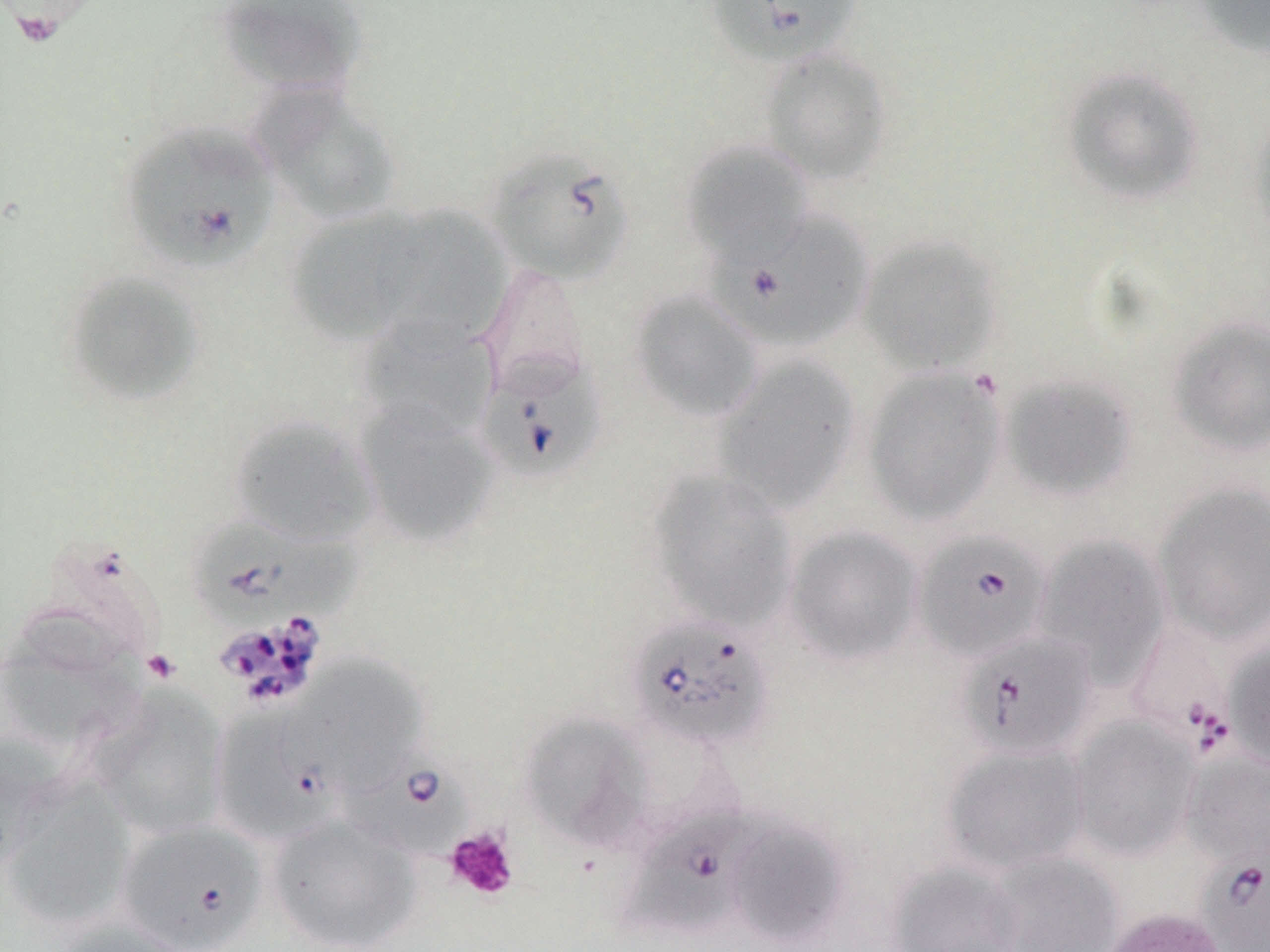
Summary:
  - Coordinate format: approximate bounding boxes as [x1, y1, x2, y2] in pixels
  - Uninfected red blood cell locations: [215, 0, 368, 98], [1192, 0, 1270, 59], [759, 47, 894, 185], [1061, 66, 1205, 206], [251, 85, 403, 226], [1247, 104, 1270, 250], [680, 139, 813, 265], [377, 204, 510, 351], [286, 208, 423, 345], [857, 234, 1004, 376], [478, 260, 592, 398], [61, 270, 207, 407], [628, 288, 765, 424], [357, 317, 499, 440], [1167, 317, 1270, 458], [711, 355, 861, 513], [861, 367, 1007, 526], [999, 374, 1139, 501], [353, 402, 500, 548], [228, 413, 379, 546], [645, 469, 798, 632], [1154, 482, 1270, 645], [784, 525, 923, 667], [1031, 533, 1171, 683], [32, 540, 165, 671], [0, 623, 144, 753], [1224, 640, 1270, 771], [285, 654, 428, 793], [89, 686, 230, 839], [519, 713, 652, 851], [1068, 715, 1201, 862], [0, 734, 60, 876], [940, 741, 1090, 874], [1181, 751, 1270, 869], [2, 779, 135, 930], [266, 813, 422, 952], [726, 818, 850, 947], [986, 851, 1124, 952], [885, 860, 1026, 952], [1101, 906, 1229, 952], [55, 918, 193, 952]
  - Platelet locations: [143, 649, 181, 685], [445, 827, 520, 901]
  - Babesia divergens-infected red blood cell locations: [706, 0, 863, 67], [120, 120, 279, 275], [486, 145, 636, 285], [715, 210, 875, 351], [475, 351, 607, 483], [190, 516, 354, 634], [913, 529, 1052, 664], [626, 614, 774, 751], [1125, 618, 1238, 756], [957, 629, 1098, 760], [210, 703, 342, 846], [339, 748, 474, 864], [622, 804, 762, 939], [115, 819, 268, 951], [1199, 851, 1270, 951]
  - Slide-level diagnosis: Babesia divergens
  - Stain: May-Grünwald-Giemsa
  - Field of view: one of a larger specimen
  - Modality: light microscopy
  - Preparation: thin blood film
  - Image size: 1270×952 pixels
  - Magnification: 1000x